Locate platelets.
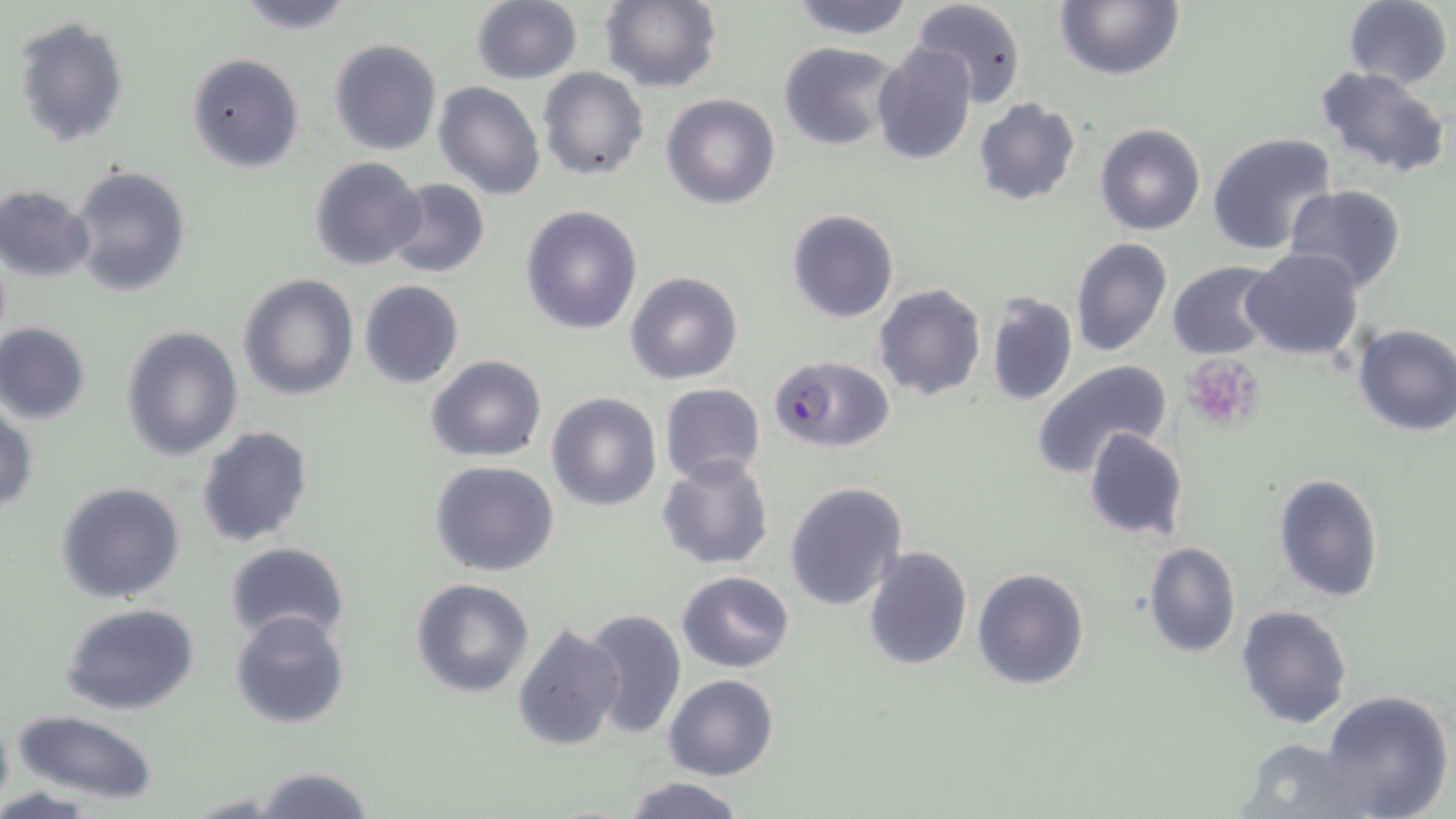

Approximate bounding boxes as [x1, y1, x2, y2] in pixels.
Platelets: [1182, 353, 1265, 434].

slide-level diagnosis = Plasmodium falciparum
image size = 1456×819 pixels
preparation = thin blood film
Plasmodium falciparum-infected red blood cell locations = approximate bounding boxes as [x1, y1, x2, y2] in pixels: [770, 355, 894, 453]
uninfected red blood cell locations = approximate bounding boxes as [x1, y1, x2, y2] in pixels: [231, 0, 359, 34], [601, 0, 723, 93], [787, 0, 916, 40], [913, 0, 1026, 108], [1053, 0, 1184, 81], [1341, 0, 1453, 86], [469, 1, 583, 84], [12, 16, 130, 148], [330, 38, 441, 155], [777, 41, 906, 151], [871, 41, 978, 166], [185, 54, 304, 172], [1314, 64, 1451, 179], [538, 67, 648, 180], [433, 81, 544, 200], [662, 94, 779, 209], [973, 98, 1082, 205], [1095, 122, 1206, 235], [1208, 131, 1340, 257], [310, 155, 425, 272], [70, 164, 191, 296], [386, 177, 489, 277], [0, 183, 96, 282], [1283, 185, 1408, 295], [520, 204, 643, 335], [787, 209, 899, 325], [1070, 237, 1172, 357], [1243, 248, 1364, 362], [1167, 261, 1280, 359], [625, 271, 743, 384], [236, 273, 360, 401], [358, 280, 464, 389], [873, 283, 988, 401], [985, 292, 1079, 408], [0, 322, 90, 423], [1352, 323, 1456, 437], [119, 324, 244, 461], [425, 355, 547, 461], [1031, 360, 1174, 480], [659, 383, 766, 487], [547, 391, 662, 510], [0, 402, 37, 516], [195, 425, 314, 548], [1083, 427, 1189, 542], [656, 453, 775, 570], [429, 460, 560, 577], [1272, 472, 1385, 603], [785, 481, 907, 610], [56, 482, 186, 603], [1142, 541, 1241, 658], [222, 543, 350, 644], [863, 546, 972, 669], [972, 567, 1090, 691], [677, 570, 795, 671], [410, 578, 535, 699], [61, 604, 201, 715], [1236, 604, 1353, 729], [230, 608, 352, 729], [579, 608, 686, 740], [512, 621, 626, 752], [664, 674, 778, 781], [1319, 689, 1452, 818], [0, 707, 14, 813], [13, 710, 159, 805], [1231, 735, 1369, 819], [251, 765, 375, 819], [621, 776, 747, 818], [182, 793, 294, 818]
magnification = 1000x
stain = May-Grünwald-Giemsa
field of view = one of a larger specimen
modality = light microscopy